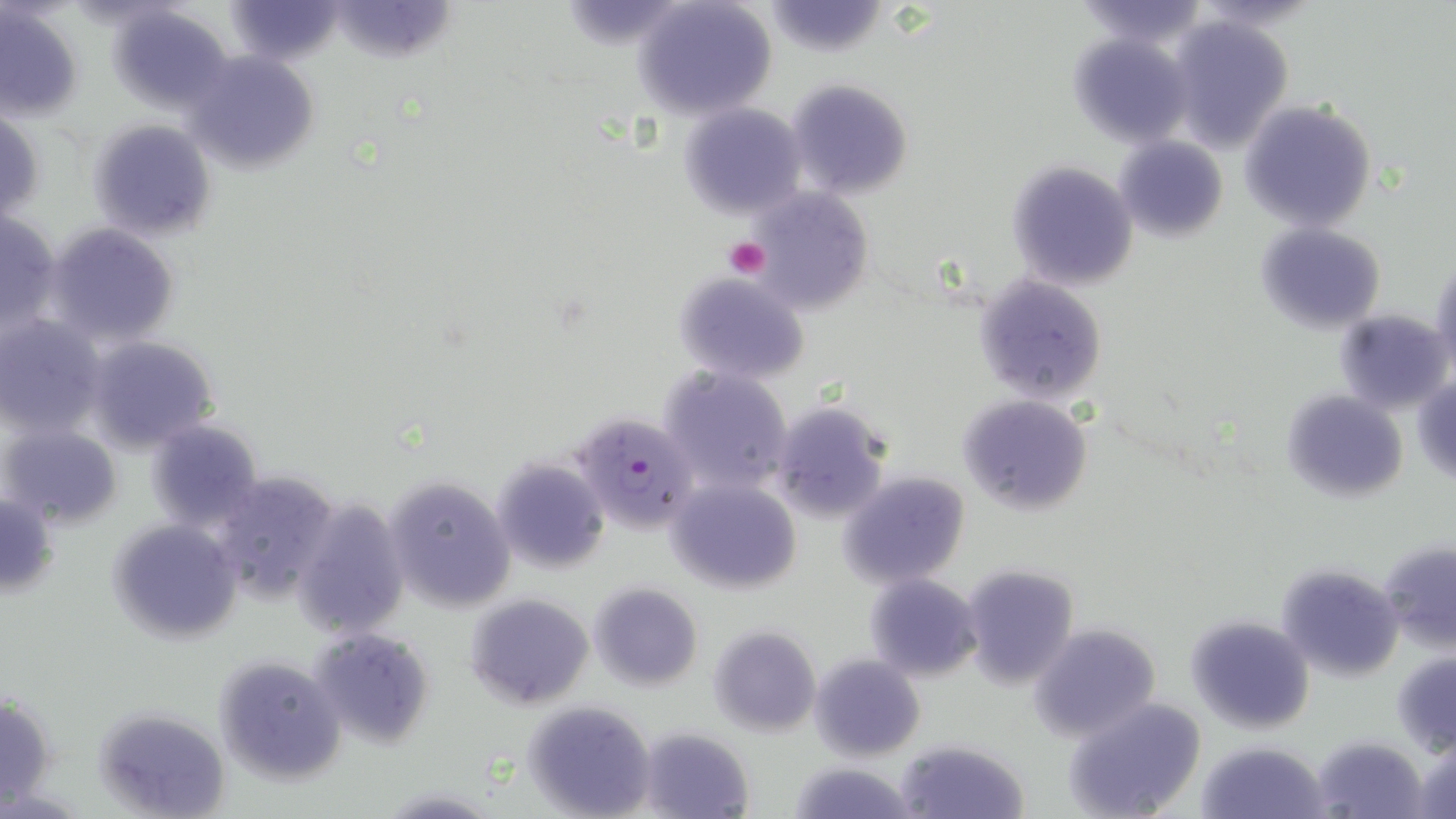
Approximate bounding boxes as [x1, y1, x2, y2] in pixels. Platelet locations: [726, 238, 770, 279]. Uninfected red blood cell locations: [229, 0, 340, 67], [327, 0, 459, 64], [633, 0, 776, 120], [1075, 0, 1206, 47], [763, 1, 889, 56], [0, 5, 83, 123], [107, 7, 232, 111], [1164, 14, 1294, 154], [1067, 31, 1193, 147], [184, 51, 320, 174], [785, 77, 915, 202], [1238, 101, 1377, 232], [678, 104, 808, 221], [0, 107, 44, 225], [87, 118, 217, 241], [1116, 137, 1228, 242], [1008, 161, 1137, 290], [747, 188, 874, 313], [1, 211, 62, 335], [1255, 220, 1387, 333], [43, 222, 180, 349], [1431, 258, 1456, 382], [672, 269, 811, 385], [975, 274, 1108, 406], [1334, 307, 1452, 415], [0, 315, 107, 440], [84, 333, 221, 454], [656, 365, 795, 495], [1412, 373, 1456, 485], [1282, 390, 1409, 504], [957, 394, 1094, 517], [768, 400, 891, 523], [146, 419, 264, 532], [0, 422, 122, 529], [492, 455, 612, 573], [212, 467, 342, 604], [838, 470, 972, 587], [383, 473, 517, 611], [667, 476, 802, 592], [0, 489, 58, 598], [290, 499, 410, 638], [107, 520, 243, 645], [1379, 540, 1456, 651], [961, 562, 1081, 689], [1276, 562, 1404, 681], [864, 574, 983, 680], [588, 582, 702, 690], [466, 593, 593, 709], [1185, 614, 1315, 736], [1029, 622, 1162, 741], [311, 625, 436, 750], [707, 625, 822, 736], [1392, 653, 1456, 754], [809, 654, 925, 760], [212, 656, 345, 786], [0, 694, 54, 811], [1064, 697, 1206, 819], [523, 699, 657, 818], [95, 709, 229, 819], [639, 728, 754, 818], [1311, 735, 1429, 818], [1410, 738, 1456, 818], [896, 739, 1029, 819], [1198, 741, 1326, 818], [788, 760, 918, 819], [378, 785, 501, 818]. Plasmodium falciparum-infected red blood cell locations: [572, 410, 700, 536]. Slide-level diagnosis: Plasmodium falciparum. May-Grünwald-Giemsa stain. Thin blood film. Image is 1456×819 pixels. Optical microscopy. One field of a larger specimen. Captured at 1000x magnification.